State which parasite is depicted.
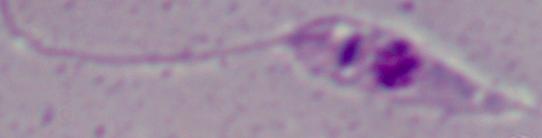
Leishmania.

modality = micrograph
magnification = 1000x